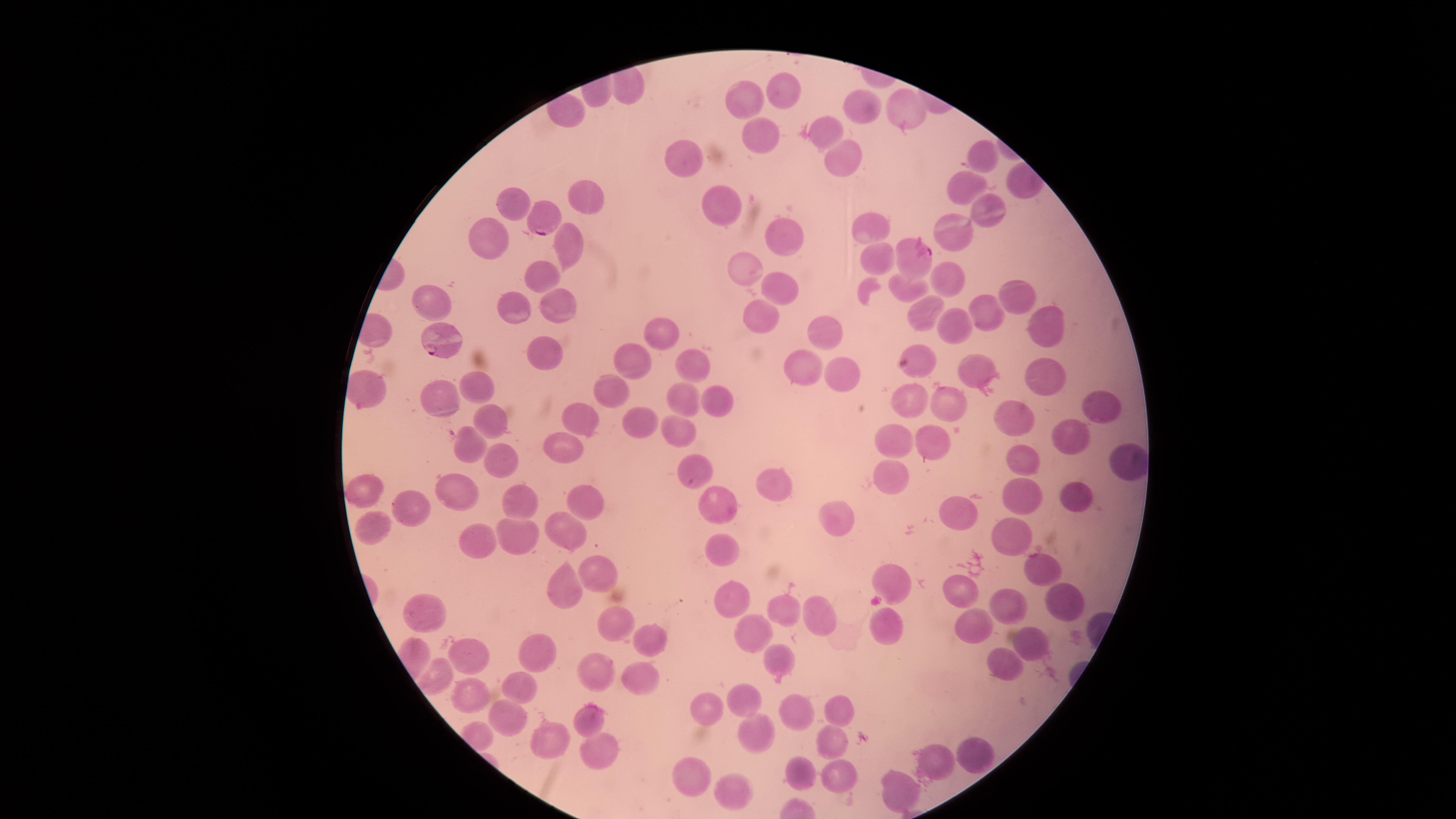

Approximate marker points as (x, y) in pixels. Parasitized RBCs: (543, 218), (914, 252), (441, 340). Uninfected RBCs: (779, 89), (751, 102), (902, 104), (866, 109), (831, 127), (760, 133), (687, 153), (838, 154), (982, 154), (967, 184), (720, 194), (595, 197), (512, 201), (987, 208), (867, 226), (957, 228), (781, 231), (499, 236), (575, 246), (874, 255), (745, 269), (542, 273), (951, 279), (781, 286), (904, 291), (1017, 292), (429, 300), (518, 303), (923, 307), (553, 308), (760, 313), (987, 314), (951, 323), (1047, 324), (662, 329), (832, 332), (544, 348), (915, 350), (633, 359), (686, 362), (803, 368), (973, 368), (848, 370), (1042, 370), (474, 386), (607, 393), (439, 396), (679, 399), (708, 399), (907, 401), (947, 401), (1095, 404), (589, 417), (1015, 420), (488, 421), (644, 428), (687, 431), (1069, 434), (889, 436), (932, 438), (469, 448), (567, 449), (1022, 456), (500, 459), (1126, 462), (693, 465), (890, 478), (777, 483), (364, 487), (461, 490), (1018, 490), (1077, 497), (587, 501), (519, 502), (416, 506), (714, 508), (961, 511), (836, 520), (372, 523), (565, 528), (1009, 536), (512, 538), (484, 539), (722, 547), (1034, 567), (599, 574), (892, 583), (964, 591), (570, 592), (730, 598), (1006, 606), (1062, 606), (782, 611), (424, 612), (822, 617), (616, 622), (974, 622), (885, 624), (750, 630), (1028, 639), (649, 641), (777, 655), (469, 656), (538, 656), (1003, 664), (593, 668), (435, 675), (643, 677), (521, 685), (468, 695), (737, 698), (704, 707), (837, 708), (797, 710), (502, 717), (584, 722), (752, 733), (550, 742), (831, 743), (597, 748), (978, 753), (933, 763), (803, 773), (840, 773), (694, 780), (737, 787), (900, 791). Smartphone photograph through the microscope eyepiece. Circular visible region. Giemsa stain. Species: Plasmodium falciparum. Single field of view. Thin blood film. Image is 1456×819 pixels. Presence: malaria parasites identified.